Report the malaria status.
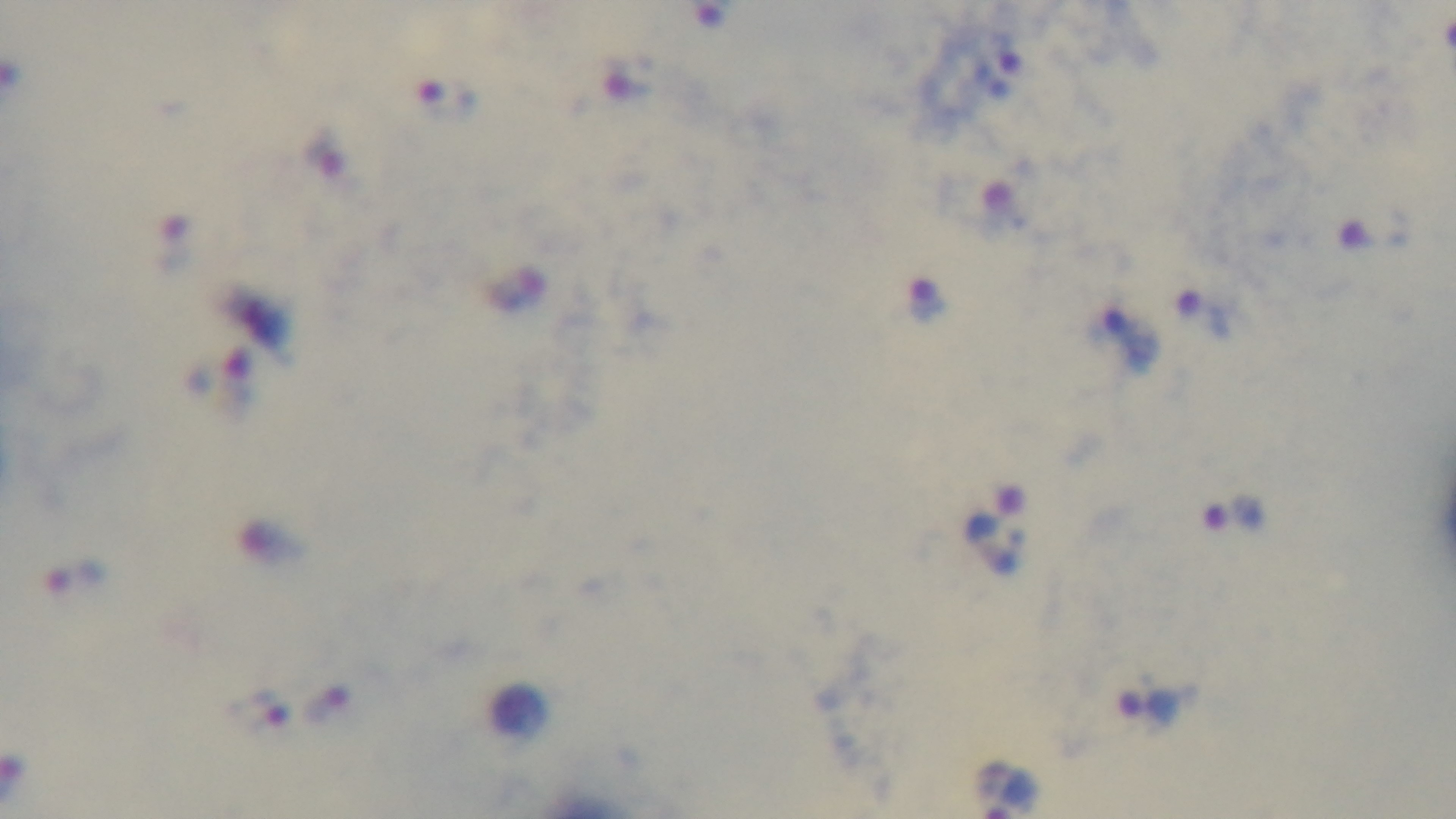
Positive.

preparation = thick blood film
field of view = single
capture = mounted 4K digital camera
stain = Giemsa
modality = light microscopy
objective = 100x oil immersion